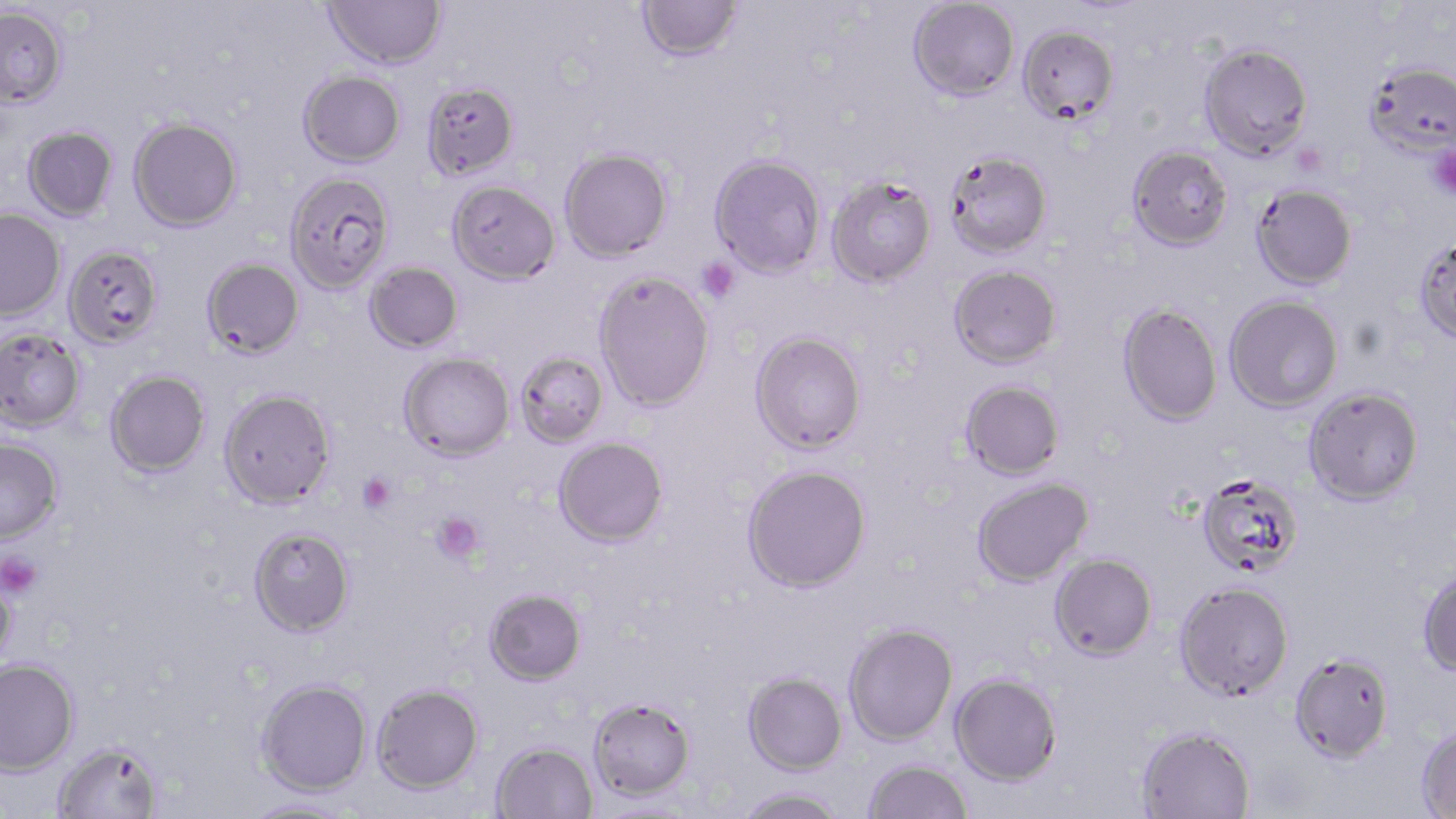

Summary:
  - Coordinate format: approximate bounding boxes as [x1, y1, x2, y2] in pixels
  - Platelet locations: [1428, 146, 1456, 199], [697, 256, 741, 303], [357, 473, 396, 514], [431, 512, 486, 565], [0, 551, 42, 599]
  - Uninfected red blood cell locations: [323, 0, 447, 70], [907, 0, 1020, 101], [636, 1, 742, 62], [0, 6, 69, 108], [1018, 26, 1119, 124], [1199, 42, 1313, 161], [1364, 60, 1456, 157], [298, 70, 406, 167], [421, 80, 519, 180], [129, 117, 243, 232], [22, 125, 118, 222], [1127, 145, 1234, 251], [559, 147, 673, 262], [944, 150, 1052, 258], [709, 154, 826, 278], [284, 172, 395, 294], [827, 175, 937, 288], [447, 180, 560, 285], [1251, 183, 1357, 290], [0, 210, 66, 323], [1414, 236, 1456, 344], [63, 245, 164, 350], [201, 258, 304, 360], [363, 262, 462, 354], [949, 264, 1062, 368], [593, 270, 715, 412], [1223, 294, 1344, 412], [1117, 303, 1223, 426], [0, 329, 85, 434], [749, 330, 866, 454], [514, 350, 608, 448], [399, 352, 515, 462], [105, 370, 210, 478], [960, 379, 1065, 480], [1304, 385, 1424, 505], [218, 388, 337, 509], [554, 437, 669, 547], [0, 440, 64, 546], [741, 463, 871, 593], [1196, 472, 1304, 579], [971, 477, 1094, 587], [248, 526, 355, 637], [1049, 552, 1157, 660], [1418, 566, 1456, 678], [0, 573, 17, 676], [1175, 580, 1294, 701], [484, 589, 587, 686], [843, 622, 958, 745], [1289, 652, 1395, 763], [0, 660, 79, 779], [742, 672, 848, 775], [950, 673, 1062, 786], [255, 680, 372, 798], [372, 685, 484, 796], [588, 697, 696, 802], [1416, 724, 1456, 817], [1136, 725, 1256, 819], [491, 743, 597, 819], [54, 744, 163, 819], [863, 759, 973, 819], [735, 787, 848, 819], [243, 799, 361, 819]
  - Slide-level diagnosis: Plasmodium falciparum
  - Image size: 1456×819 pixels
  - Field of view: single
  - Magnification: 1000x
  - Preparation: thin blood smear
  - Modality: light microscopy
  - Stain: May-Grünwald-Giemsa